Classify this cell by malaria status.
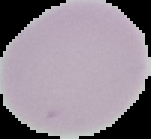
It is uninfected.

The area outside the segmented cell region is set to black. Image is 151×139 pixels. From a thin blood film.